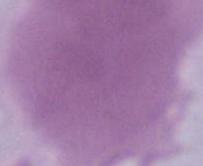

identification = red blood cell
modality = micrograph
magnification = 1000x